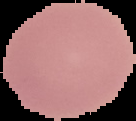
image type = segmented cell region with the area outside set to black
preparation = thin blood smear
result = no Plasmodium parasites seen
image size = 136×121 pixels